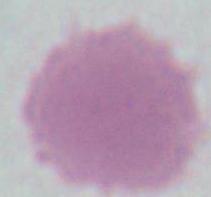
Summary:
  - Modality: micrograph
  - Identification: red blood cell
  - Magnification: 1000x